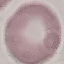 Malaria status: uninfected. Giemsa stain. Thin smear of blood. Automatically extracted cell patch, resized to 64 × 64 pixels. Photographed with a smartphone camera at the microscope eyepiece.